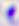
Summary:
  - Identification: Toxoplasma gondii
  - Magnification: 400x
  - Modality: micrograph